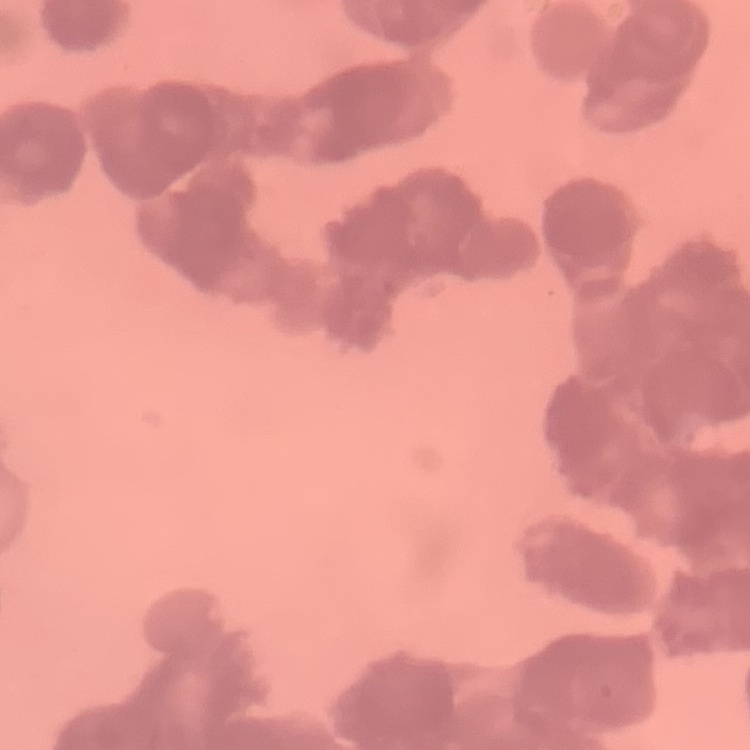 The red blood cells show rouleaux formation. Field's or Giemsa stain. Square crop of a larger photomicrograph. Thin blood film.